State which cell type is depicted.
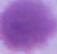

This is an erythrocyte.

modality = micrograph
magnification = 1000x